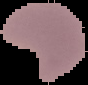
From a thin blood film. Image is 88×85 pixels. The area outside the segmented cell region is set to black. Malaria status: parasitized.